Locate every cell, classifying each as a parasitized red blood cell, an uninfected red blood cell, or a white blood cell.
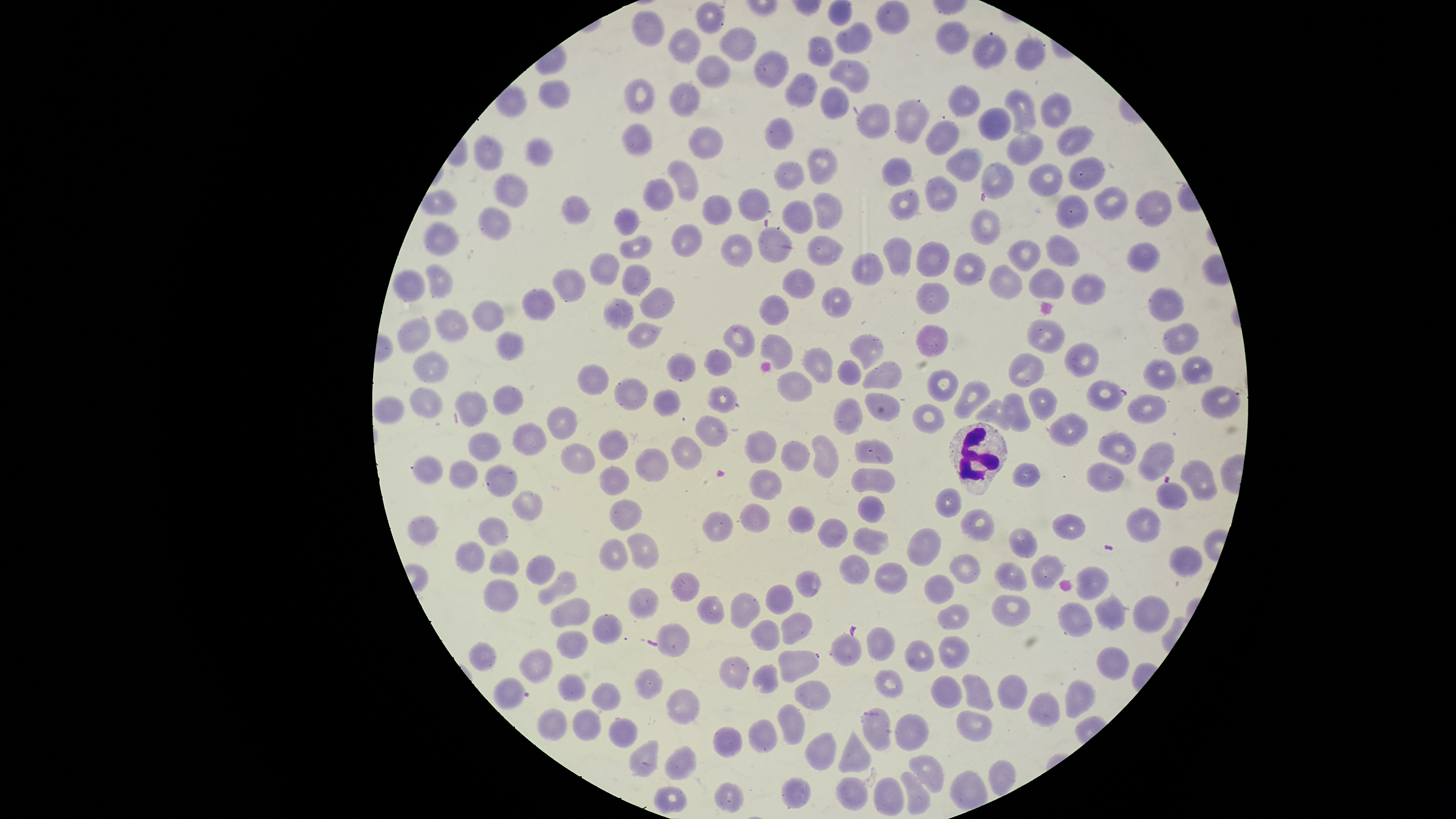
Approximate bounding boxes, in pixels from the top-left corner.
Parasitized red blood cells: (left=1085, top=379, right=1128, bottom=412), (left=493, top=676, right=530, bottom=711).
Uninfected red blood cells: (left=827, top=0, right=853, bottom=26), (left=696, top=2, right=727, bottom=34), (left=877, top=2, right=910, bottom=34), (left=633, top=9, right=665, bottom=47), (left=836, top=20, right=872, bottom=54), (left=935, top=21, right=969, bottom=55), (left=669, top=27, right=701, bottom=62), (left=718, top=27, right=757, bottom=61), (left=972, top=31, right=1007, bottom=70), (left=808, top=36, right=835, bottom=68), (left=1015, top=36, right=1047, bottom=70), (left=754, top=50, right=788, bottom=88), (left=697, top=54, right=731, bottom=87), (left=830, top=60, right=871, bottom=93), (left=786, top=74, right=816, bottom=108), (left=624, top=78, right=655, bottom=114), (left=539, top=80, right=572, bottom=110), (left=670, top=82, right=701, bottom=117), (left=947, top=84, right=981, bottom=117), (left=821, top=87, right=850, bottom=120), (left=1005, top=88, right=1037, bottom=135), (left=1042, top=92, right=1071, bottom=128), (left=895, top=100, right=930, bottom=143), (left=856, top=103, right=890, bottom=138), (left=978, top=107, right=1013, bottom=140), (left=764, top=117, right=794, bottom=149), (left=926, top=118, right=959, bottom=155), (left=622, top=124, right=653, bottom=158), (left=1056, top=124, right=1093, bottom=155), (left=690, top=127, right=723, bottom=160), (left=1007, top=130, right=1044, bottom=164), (left=473, top=135, right=503, bottom=170), (left=524, top=138, right=553, bottom=167), (left=807, top=148, right=838, bottom=185), (left=946, top=148, right=981, bottom=181), (left=1067, top=156, right=1106, bottom=191), (left=882, top=157, right=912, bottom=186), (left=667, top=160, right=699, bottom=201), (left=981, top=160, right=1014, bottom=200), (left=774, top=161, right=804, bottom=190), (left=1027, top=162, right=1063, bottom=195), (left=495, top=171, right=529, bottom=208), (left=924, top=177, right=959, bottom=212), (left=642, top=178, right=673, bottom=210), (left=1093, top=187, right=1128, bottom=220), (left=738, top=188, right=769, bottom=221), (left=889, top=189, right=919, bottom=221), (left=420, top=190, right=457, bottom=215), (left=1136, top=191, right=1174, bottom=225), (left=813, top=192, right=844, bottom=230), (left=1055, top=194, right=1089, bottom=227), (left=561, top=195, right=591, bottom=225), (left=703, top=195, right=733, bottom=225), (left=782, top=198, right=813, bottom=234), (left=477, top=205, right=512, bottom=240), (left=613, top=207, right=640, bottom=237), (left=969, top=210, right=1002, bottom=245), (left=422, top=220, right=461, bottom=256), (left=672, top=224, right=701, bottom=257), (left=758, top=225, right=792, bottom=264), (left=620, top=233, right=652, bottom=260), (left=721, top=233, right=752, bottom=266), (left=808, top=235, right=843, bottom=266), (left=882, top=236, right=912, bottom=276), (left=1045, top=236, right=1080, bottom=265), (left=1007, top=241, right=1041, bottom=273), (left=1128, top=241, right=1161, bottom=273), (left=916, top=242, right=949, bottom=278), (left=589, top=252, right=620, bottom=285), (left=852, top=253, right=884, bottom=285), (left=954, top=253, right=985, bottom=287), (left=426, top=263, right=454, bottom=297), (left=621, top=264, right=651, bottom=296), (left=989, top=266, right=1023, bottom=299), (left=393, top=268, right=425, bottom=302), (left=553, top=268, right=586, bottom=302), (left=782, top=268, right=815, bottom=299), (left=1028, top=268, right=1064, bottom=300), (left=1071, top=273, right=1107, bottom=305), (left=916, top=283, right=949, bottom=315), (left=523, top=287, right=555, bottom=320), (left=640, top=287, right=676, bottom=320), (left=822, top=287, right=853, bottom=318), (left=1148, top=287, right=1184, bottom=321), (left=760, top=295, right=789, bottom=325), (left=604, top=297, right=635, bottom=329), (left=473, top=299, right=504, bottom=331), (left=436, top=308, right=470, bottom=342), (left=397, top=317, right=430, bottom=355), (left=1026, top=320, right=1064, bottom=354), (left=628, top=322, right=662, bottom=348), (left=723, top=323, right=755, bottom=359), (left=1161, top=323, right=1200, bottom=354), (left=915, top=325, right=948, bottom=360), (left=496, top=332, right=524, bottom=360), (left=761, top=333, right=792, bottom=370), (left=850, top=334, right=883, bottom=369), (left=1064, top=341, right=1100, bottom=378), (left=803, top=348, right=833, bottom=385), (left=704, top=349, right=733, bottom=377), (left=414, top=350, right=449, bottom=382), (left=667, top=352, right=696, bottom=382), (left=1009, top=353, right=1045, bottom=389), (left=1182, top=356, right=1214, bottom=384), (left=838, top=358, right=861, bottom=386), (left=1143, top=359, right=1176, bottom=391), (left=863, top=360, right=902, bottom=389), (left=578, top=365, right=609, bottom=395), (left=777, top=371, right=813, bottom=402), (left=927, top=371, right=958, bottom=403), (left=614, top=378, right=647, bottom=410), (left=955, top=380, right=991, bottom=420), (left=707, top=385, right=738, bottom=413), (left=1201, top=385, right=1241, bottom=419), (left=493, top=386, right=524, bottom=415), (left=1027, top=386, right=1059, bottom=421), (left=411, top=387, right=444, bottom=418), (left=653, top=389, right=681, bottom=417), (left=456, top=390, right=488, bottom=427), (left=864, top=391, right=901, bottom=421), (left=1001, top=393, right=1031, bottom=430), (left=1129, top=394, right=1168, bottom=424), (left=374, top=396, right=406, bottom=426), (left=834, top=397, right=862, bottom=435), (left=974, top=399, right=1012, bottom=430), (left=912, top=401, right=945, bottom=436), (left=548, top=405, right=578, bottom=440), (left=1049, top=413, right=1089, bottom=449), (left=696, top=415, right=729, bottom=447), (left=513, top=422, right=546, bottom=456), (left=597, top=429, right=628, bottom=461), (left=746, top=431, right=777, bottom=464), (left=1099, top=431, right=1137, bottom=466), (left=468, top=432, right=501, bottom=461), (left=811, top=435, right=838, bottom=480), (left=670, top=436, right=703, bottom=470), (left=855, top=439, right=893, bottom=464), (left=781, top=441, right=810, bottom=472), (left=1138, top=442, right=1175, bottom=480), (left=559, top=444, right=595, bottom=475), (left=634, top=447, right=669, bottom=482), (left=412, top=456, right=443, bottom=484), (left=448, top=459, right=478, bottom=489), (left=1181, top=459, right=1219, bottom=500), (left=1010, top=462, right=1041, bottom=489), (left=1087, top=462, right=1124, bottom=492), (left=485, top=464, right=518, bottom=497), (left=598, top=466, right=630, bottom=496), (left=851, top=467, right=895, bottom=492), (left=749, top=468, right=782, bottom=500), (left=1156, top=481, right=1189, bottom=509), (left=936, top=488, right=963, bottom=519), (left=513, top=490, right=543, bottom=522), (left=858, top=495, right=884, bottom=523), (left=610, top=498, right=642, bottom=530), (left=741, top=503, right=770, bottom=533), (left=789, top=506, right=816, bottom=533), (left=1126, top=507, right=1162, bottom=542), (left=961, top=508, right=994, bottom=542), (left=702, top=511, right=733, bottom=542), (left=407, top=514, right=438, bottom=547), (left=1051, top=515, right=1085, bottom=539), (left=479, top=517, right=509, bottom=546), (left=817, top=518, right=847, bottom=548), (left=852, top=527, right=890, bottom=555), (left=1009, top=527, right=1038, bottom=558), (left=906, top=528, right=941, bottom=568), (left=627, top=533, right=660, bottom=569), (left=599, top=538, right=629, bottom=572), (left=456, top=541, right=486, bottom=573), (left=1169, top=546, right=1203, bottom=578), (left=490, top=547, right=519, bottom=576), (left=949, top=552, right=982, bottom=583), (left=527, top=554, right=555, bottom=586), (left=839, top=554, right=870, bottom=586), (left=1030, top=554, right=1066, bottom=589), (left=994, top=561, right=1027, bottom=591), (left=875, top=563, right=908, bottom=594), (left=1076, top=565, right=1111, bottom=601), (left=796, top=570, right=821, bottom=597), (left=538, top=571, right=577, bottom=605), (left=672, top=572, right=701, bottom=602), (left=924, top=575, right=954, bottom=604), (left=484, top=579, right=519, bottom=612), (left=766, top=585, right=794, bottom=615), (left=630, top=587, right=660, bottom=620), (left=731, top=592, right=760, bottom=628), (left=1094, top=593, right=1126, bottom=629), (left=696, top=595, right=724, bottom=626), (left=992, top=595, right=1030, bottom=628), (left=1132, top=595, right=1169, bottom=634), (left=550, top=598, right=590, bottom=629), (left=1056, top=600, right=1092, bottom=638), (left=937, top=603, right=970, bottom=633), (left=782, top=613, right=814, bottom=646), (left=592, top=614, right=622, bottom=646), (left=752, top=620, right=781, bottom=650), (left=655, top=624, right=690, bottom=658), (left=867, top=626, right=896, bottom=662), (left=556, top=630, right=589, bottom=660), (left=831, top=631, right=862, bottom=666), (left=939, top=636, right=970, bottom=669), (left=905, top=640, right=936, bottom=672), (left=468, top=642, right=496, bottom=671), (left=1095, top=645, right=1130, bottom=681), (left=520, top=648, right=554, bottom=684), (left=777, top=649, right=819, bottom=682), (left=718, top=655, right=750, bottom=689), (left=753, top=663, right=778, bottom=692), (left=635, top=668, right=663, bottom=699), (left=874, top=670, right=905, bottom=697), (left=997, top=673, right=1027, bottom=710), (left=558, top=674, right=586, bottom=702), (left=962, top=674, right=995, bottom=712), (left=931, top=675, right=962, bottom=710), (left=1064, top=678, right=1095, bottom=719), (left=795, top=682, right=830, bottom=709), (left=593, top=683, right=622, bottom=711), (left=666, top=688, right=700, bottom=726), (left=1029, top=692, right=1061, bottom=726), (left=778, top=704, right=805, bottom=746), (left=862, top=708, right=891, bottom=750), (left=536, top=709, right=568, bottom=741), (left=573, top=710, right=603, bottom=741), (left=957, top=710, right=993, bottom=743), (left=895, top=715, right=929, bottom=752), (left=610, top=717, right=638, bottom=749), (left=748, top=719, right=776, bottom=753), (left=713, top=727, right=741, bottom=757), (left=839, top=729, right=871, bottom=774), (left=803, top=731, right=836, bottom=771), (left=630, top=740, right=659, bottom=776), (left=665, top=745, right=696, bottom=781), (left=909, top=754, right=945, bottom=792), (left=900, top=771, right=929, bottom=814), (left=781, top=776, right=811, bottom=809), (left=836, top=776, right=868, bottom=808), (left=873, top=776, right=903, bottom=815), (left=715, top=782, right=744, bottom=811), (left=655, top=786, right=687, bottom=813).
White blood cells: (left=947, top=422, right=1009, bottom=496).

Image is 1456×819 pixels. Smartphone photograph through the microscope eyepiece. Circular visible region. One field of view of the specimen. Giemsa stain. Thin blood film. Species: Plasmodium falciparum.